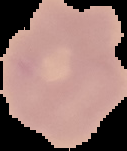

Summary:
  - Preparation: thin blood film
  - Image type: cell region segmented out of the field of view; surrounding area masked to black
  - Malaria status: uninfected
  - Image size: 127×151 pixels